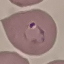
malaria status = parasitized
preparation = thin blood smear
stain = Giemsa
capture = smartphone through the microscope eyepiece
image type = cell patch, automatically extracted from a larger field of view and resized to 64 × 64 pixels